Report the malaria status of this cell.
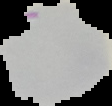

Uninfected.

Summary:
  - Preparation: thin blood smear
  - Image size: 112×106 pixels
  - Image type: segmented cell region with the area outside set to black